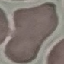
Summary:
  - Result: no malaria parasites detected
  - Stain: Giemsa
  - Capture: smartphone through the microscope eyepiece
  - Preparation: thin smear
  - Image type: cell patch, automatically extracted from a larger field of view and resized to 64 × 64 pixels